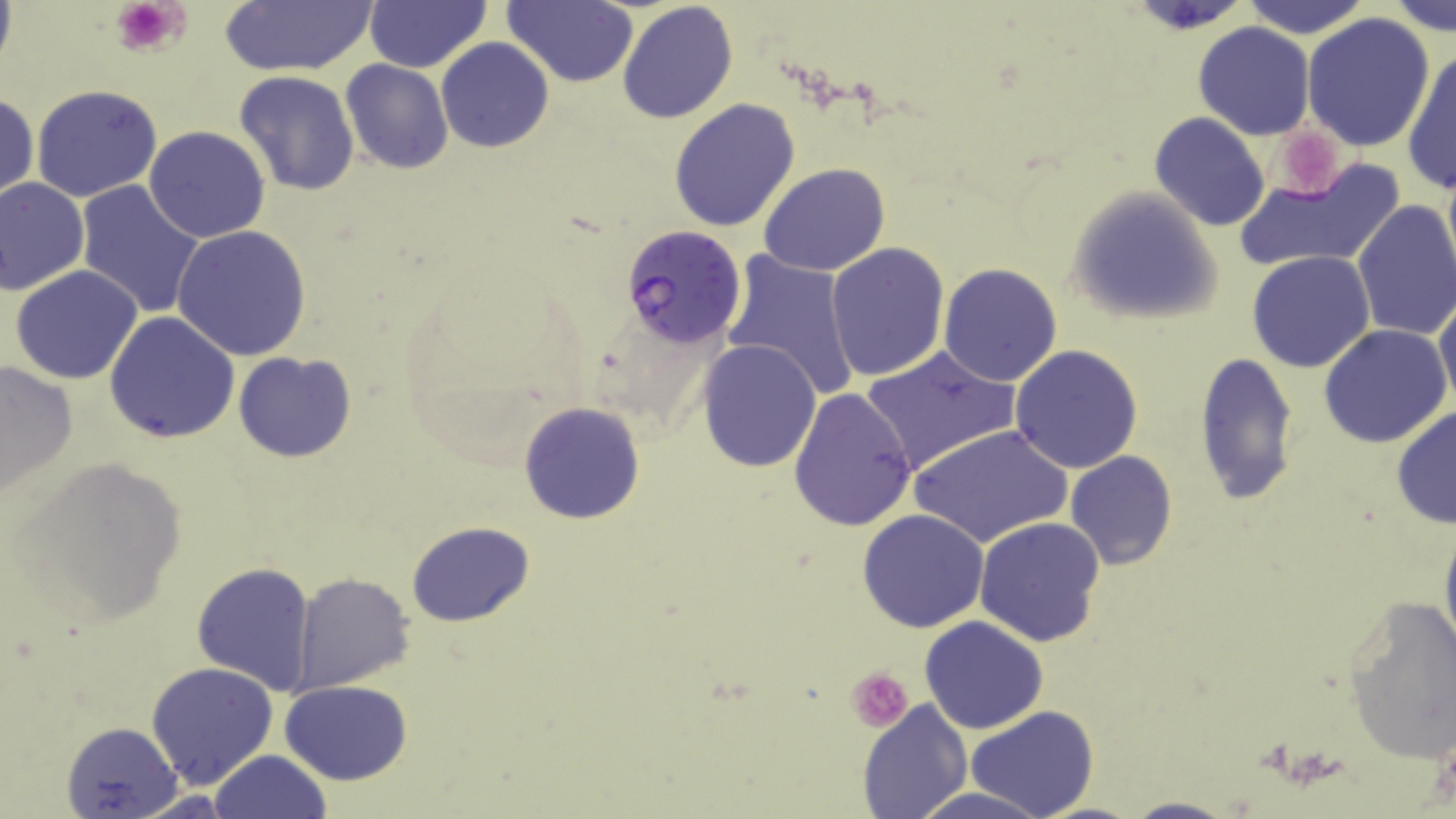
Summary:
  - Coordinate format: approximate bounding boxes as [x1, y1, x2, y2] in pixels
  - Uninfected red blood cell locations: [363, 0, 491, 73], [504, 0, 639, 87], [1239, 0, 1370, 36], [1386, 0, 1454, 35], [220, 1, 376, 76], [616, 2, 739, 124], [1301, 11, 1435, 153], [1193, 22, 1315, 139], [435, 38, 556, 153], [1401, 47, 1456, 195], [340, 59, 453, 174], [234, 71, 361, 195], [29, 83, 163, 202], [1, 92, 38, 204], [668, 98, 802, 233], [1150, 112, 1270, 230], [144, 125, 271, 243], [1232, 157, 1405, 275], [759, 163, 889, 277], [0, 176, 89, 296], [74, 181, 206, 319], [1066, 187, 1222, 324], [1352, 199, 1456, 342], [170, 225, 314, 360], [825, 241, 950, 381], [722, 251, 860, 403], [1246, 251, 1375, 374], [938, 263, 1064, 387], [9, 264, 146, 384], [1434, 293, 1456, 410], [104, 312, 240, 445], [1319, 324, 1452, 448], [696, 338, 822, 472], [862, 344, 1018, 477], [1009, 344, 1143, 473], [232, 350, 358, 463], [1193, 351, 1300, 506], [1, 358, 77, 500], [788, 386, 919, 532], [517, 401, 645, 525], [1390, 407, 1456, 529], [912, 423, 1072, 549], [1065, 451, 1178, 569], [10, 456, 189, 633], [858, 509, 989, 632], [975, 516, 1106, 646], [1438, 518, 1456, 665], [405, 521, 533, 627], [193, 562, 315, 693], [294, 572, 416, 693], [1342, 594, 1456, 764], [920, 616, 1049, 734], [145, 662, 279, 790], [281, 680, 411, 785], [858, 699, 972, 818], [967, 708, 1098, 819], [60, 721, 182, 819], [210, 748, 331, 819], [910, 786, 1046, 819], [1118, 796, 1240, 819]
  - Platelet locations: [111, 0, 189, 57], [1278, 133, 1349, 194], [847, 667, 912, 731]
  - Plasmodium falciparum-infected red blood cell locations: [619, 226, 747, 350]
  - Slide-level diagnosis: Plasmodium falciparum
  - Preparation: thin blood smear
  - Modality: light microscopy
  - Image size: 1456×819 pixels
  - Field of view: one of a larger specimen
  - Magnification: 1000x
  - Stain: May-Grünwald-Giemsa